Identify the parasite.
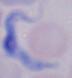

A trypanosome.

modality = micrograph
magnification = 1000x